Assess this cell for malaria.
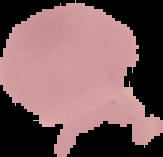

It is uninfected.

image_size: 163×157 pixels
preparation: thin blood film
image_type: cell region segmented out of the field of view; surrounding area masked to black